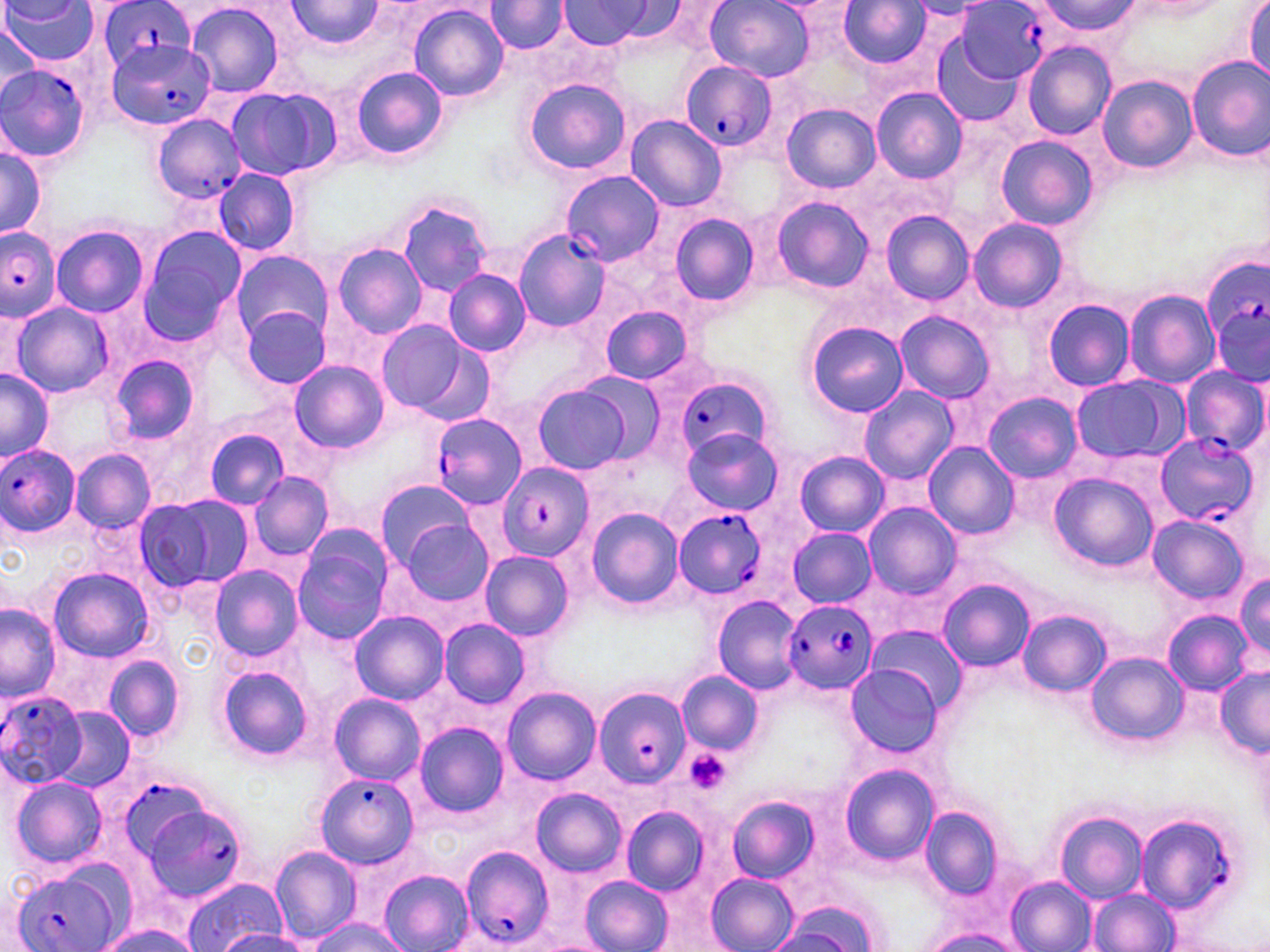

slide_level_diagnosis: Plasmodium falciparum
stain: May-Grünwald-Giemsa
field_of_view: single
preparation: thin blood film
platelet_locations: 'approximate bounding boxes as (x1, y1, x2, y2) in pixels: (684, 748, 733, 796)'
modality: light microscopy
uninfected_red_blood_cell_locations: 'approximate bounding boxes as (x1, y1, x2, y2) in pixels: (287, 0, 386, 48), (705, 0, 815, 81), (1244, 0, 1270, 84), (3, 1, 98, 64), (840, 1, 929, 67), (185, 2, 283, 99), (486, 2, 569, 55), (559, 2, 656, 48), (1032, 2, 1143, 39), (407, 4, 508, 102), (0, 21, 40, 110), (929, 31, 1027, 127), (1022, 44, 1115, 140), (1186, 55, 1270, 164), (351, 66, 448, 162), (1097, 74, 1197, 174), (525, 78, 632, 175), (871, 87, 968, 184), (225, 88, 331, 180), (782, 104, 880, 193), (626, 115, 725, 211), (996, 134, 1097, 231), (0, 146, 45, 238), (215, 168, 300, 257), (772, 195, 873, 293), (395, 198, 497, 297), (881, 211, 973, 305), (669, 212, 760, 305), (968, 217, 1068, 312), (51, 224, 149, 318), (139, 224, 243, 341), (331, 243, 427, 338), (232, 251, 332, 339), (443, 270, 531, 357), (1125, 289, 1218, 389), (1042, 299, 1134, 391), (9, 301, 116, 398), (598, 303, 697, 384), (241, 304, 332, 389), (895, 310, 995, 404), (1212, 313, 1268, 383), (375, 318, 489, 422), (806, 321, 908, 419), (108, 355, 200, 446), (289, 361, 388, 454), (0, 369, 53, 464), (576, 372, 669, 462), (1070, 376, 1180, 466), (532, 384, 634, 474), (858, 385, 958, 486), (983, 391, 1080, 482), (202, 426, 293, 508), (681, 427, 784, 516), (925, 441, 1022, 540), (70, 449, 156, 533), (796, 451, 889, 536), (246, 470, 333, 562), (1050, 472, 1159, 572), (375, 478, 473, 571), (135, 497, 251, 592), (863, 502, 960, 599), (586, 507, 686, 610), (399, 516, 495, 608), (1149, 516, 1247, 603), (291, 527, 392, 646), (787, 527, 877, 608), (480, 550, 573, 641), (209, 566, 304, 660), (47, 568, 155, 660), (1233, 571, 1270, 658), (936, 579, 1035, 672), (712, 594, 802, 694), (0, 604, 61, 700), (1019, 609, 1111, 697), (349, 610, 449, 705), (1163, 610, 1254, 694), (438, 619, 530, 709), (867, 627, 967, 715), (1087, 652, 1188, 746), (104, 654, 186, 745), (844, 663, 944, 757), (215, 666, 314, 760), (1215, 667, 1270, 755), (677, 669, 761, 755), (501, 687, 601, 785), (329, 693, 425, 784), (50, 708, 133, 792), (412, 722, 508, 817), (838, 764, 940, 866), (10, 775, 107, 867), (532, 789, 627, 876), (727, 796, 819, 881), (918, 805, 1004, 899), (620, 806, 710, 896), (1054, 811, 1148, 902), (269, 847, 361, 943), (378, 870, 474, 952), (706, 872, 798, 952), (580, 874, 673, 952), (1006, 875, 1097, 952), (182, 878, 285, 951), (1087, 889, 1178, 951), (771, 904, 875, 951), (306, 918, 411, 952), (98, 924, 203, 952), (921, 925, 1027, 952), (213, 929, 308, 952)'
magnification: 1000x
plasmodium_falciparum_infected_red_blood_cell_locations: 'approximate bounding boxes as (x1, y1, x2, y2) in pixels: (95, 0, 197, 69), (955, 2, 1053, 83), (109, 39, 217, 131), (681, 59, 777, 151), (1, 63, 92, 163), (150, 114, 246, 204), (562, 173, 663, 267), (0, 227, 61, 321), (515, 228, 608, 333), (1201, 251, 1270, 362), (1180, 366, 1269, 456), (679, 378, 773, 463), (431, 410, 526, 508), (1153, 432, 1258, 528), (0, 442, 81, 538), (500, 462, 593, 561), (674, 509, 768, 600), (786, 600, 877, 695), (594, 687, 692, 787), (0, 691, 86, 787), (683, 744, 736, 795), (314, 772, 418, 869), (125, 783, 214, 866), (139, 801, 250, 902), (1133, 811, 1242, 916), (458, 845, 556, 949), (9, 866, 124, 952)'
image_size: 1270×952 pixels